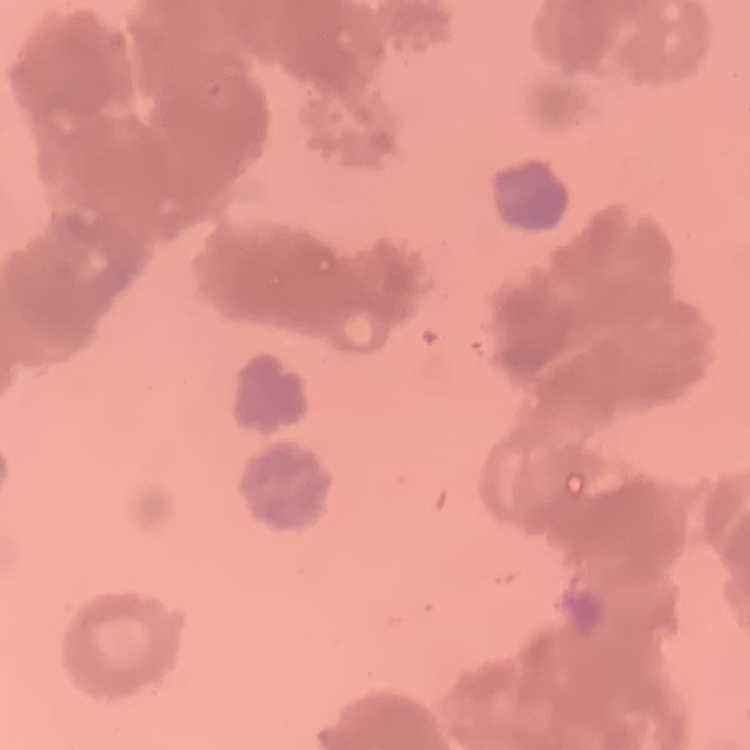

{
  "erythrocyte_morphology": "rouleaux formation",
  "image_type": "one tile cut from a larger photomicrograph",
  "stain": "Field's or Giemsa",
  "preparation": "thin peripheral smear"
}